Locate and identify every blood parasite.
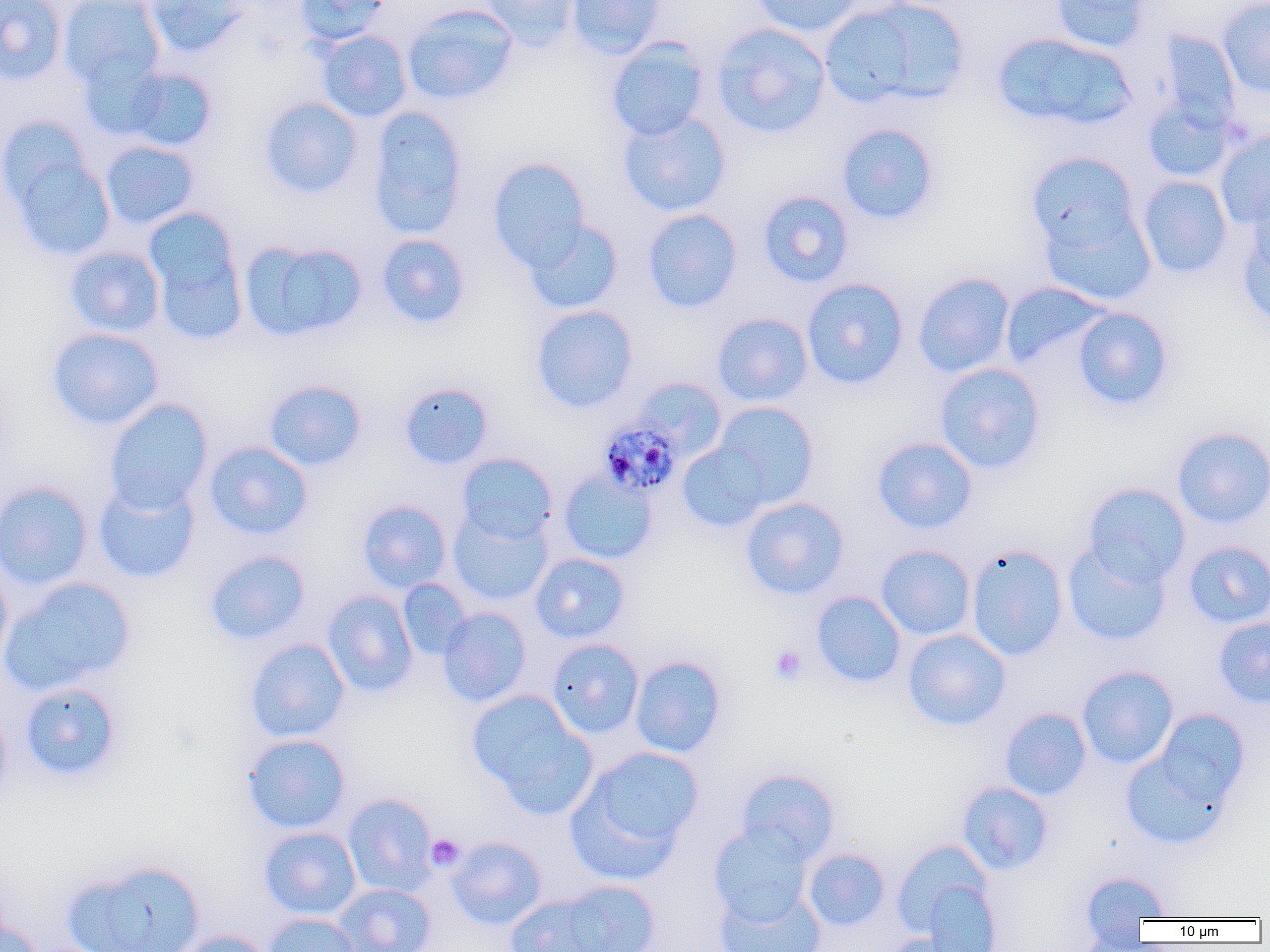

Approximate bounding boxes as named x1/y1/x2/y2 corners in pixels.
Plasmodium malariae-infected red blood cells: (x1=597, y1=417, x2=683, y2=498).
No Plasmodium falciparum, Plasmodium ovale, Plasmodium vivax, Babesia divergens, or Trypanosoma brucei observed.

slide-level diagnosis = Plasmodium malariae
platelet locations = approximate bounding boxes as named x1/y1/x2/y2 corners in pixels: (x1=769, y1=645, x2=809, y2=686), (x1=425, y1=834, x2=465, y2=872)
preparation = thin blood smear
modality = light microscopy
magnification = 1000x
image size = 1270×952 pixels
field of view = single
uninfected red blood cell locations = approximate bounding boxes as named x1/y1/x2/y2 corners in pixels: (x1=0, y1=0, x2=67, y2=86), (x1=58, y1=0, x2=166, y2=89), (x1=143, y1=0, x2=248, y2=58), (x1=295, y1=0, x2=393, y2=46), (x1=479, y1=0, x2=583, y2=48), (x1=565, y1=0, x2=666, y2=59), (x1=749, y1=0, x2=866, y2=37), (x1=819, y1=0, x2=969, y2=111), (x1=1050, y1=0, x2=1156, y2=52), (x1=1218, y1=0, x2=1270, y2=98), (x1=401, y1=4, x2=519, y2=105), (x1=711, y1=23, x2=832, y2=139), (x1=1156, y1=29, x2=1241, y2=129), (x1=317, y1=30, x2=413, y2=122), (x1=991, y1=31, x2=1137, y2=131), (x1=605, y1=37, x2=711, y2=142), (x1=77, y1=56, x2=172, y2=142), (x1=119, y1=66, x2=218, y2=152), (x1=259, y1=96, x2=363, y2=198), (x1=1142, y1=97, x2=1235, y2=184), (x1=365, y1=105, x2=469, y2=238), (x1=618, y1=110, x2=732, y2=217), (x1=835, y1=123, x2=941, y2=225), (x1=1214, y1=131, x2=1270, y2=229), (x1=4, y1=137, x2=116, y2=262), (x1=100, y1=140, x2=199, y2=230), (x1=1025, y1=151, x2=1141, y2=256), (x1=487, y1=157, x2=590, y2=271), (x1=1137, y1=175, x2=1232, y2=279), (x1=1246, y1=179, x2=1270, y2=280), (x1=757, y1=191, x2=855, y2=288), (x1=1039, y1=203, x2=1157, y2=307), (x1=641, y1=208, x2=743, y2=313), (x1=145, y1=210, x2=245, y2=341), (x1=523, y1=219, x2=624, y2=314), (x1=1237, y1=226, x2=1270, y2=328), (x1=375, y1=233, x2=471, y2=329), (x1=239, y1=238, x2=367, y2=342), (x1=64, y1=245, x2=165, y2=337), (x1=913, y1=272, x2=1016, y2=378), (x1=802, y1=277, x2=909, y2=390), (x1=999, y1=281, x2=1110, y2=369), (x1=530, y1=304, x2=639, y2=413), (x1=1072, y1=307, x2=1174, y2=411), (x1=712, y1=312, x2=814, y2=407), (x1=47, y1=327, x2=164, y2=430), (x1=934, y1=362, x2=1046, y2=475), (x1=633, y1=377, x2=728, y2=460), (x1=263, y1=379, x2=367, y2=472), (x1=399, y1=382, x2=494, y2=470), (x1=104, y1=398, x2=213, y2=512), (x1=709, y1=401, x2=819, y2=510), (x1=1171, y1=426, x2=1270, y2=529), (x1=872, y1=436, x2=978, y2=534), (x1=203, y1=440, x2=314, y2=541), (x1=677, y1=440, x2=773, y2=532), (x1=456, y1=452, x2=557, y2=545), (x1=558, y1=470, x2=658, y2=565), (x1=92, y1=477, x2=201, y2=584), (x1=1, y1=480, x2=94, y2=592), (x1=1081, y1=483, x2=1191, y2=587), (x1=740, y1=497, x2=849, y2=601), (x1=357, y1=499, x2=452, y2=593), (x1=449, y1=508, x2=553, y2=607), (x1=1062, y1=540, x2=1171, y2=646), (x1=1183, y1=541, x2=1270, y2=628), (x1=966, y1=544, x2=1069, y2=661), (x1=876, y1=545, x2=975, y2=640), (x1=203, y1=549, x2=311, y2=646), (x1=530, y1=552, x2=631, y2=644), (x1=0, y1=565, x2=13, y2=675), (x1=1, y1=576, x2=136, y2=696), (x1=397, y1=578, x2=472, y2=660), (x1=322, y1=590, x2=418, y2=697), (x1=811, y1=591, x2=906, y2=688), (x1=437, y1=607, x2=533, y2=708), (x1=1213, y1=616, x2=1270, y2=708), (x1=902, y1=629, x2=1011, y2=731), (x1=244, y1=638, x2=350, y2=743), (x1=546, y1=638, x2=644, y2=738), (x1=629, y1=655, x2=727, y2=758), (x1=1077, y1=665, x2=1179, y2=769), (x1=18, y1=682, x2=123, y2=782), (x1=466, y1=689, x2=594, y2=812), (x1=0, y1=706, x2=12, y2=808), (x1=999, y1=707, x2=1092, y2=801), (x1=1139, y1=707, x2=1250, y2=830), (x1=241, y1=733, x2=351, y2=835), (x1=569, y1=746, x2=704, y2=876), (x1=1119, y1=747, x2=1231, y2=851), (x1=735, y1=768, x2=840, y2=864), (x1=956, y1=781, x2=1054, y2=876), (x1=342, y1=793, x2=438, y2=897), (x1=709, y1=823, x2=814, y2=925), (x1=259, y1=826, x2=361, y2=920), (x1=447, y1=837, x2=546, y2=929), (x1=891, y1=839, x2=997, y2=942), (x1=802, y1=847, x2=891, y2=932), (x1=63, y1=859, x2=206, y2=952), (x1=1079, y1=871, x2=1172, y2=938), (x1=914, y1=875, x2=1004, y2=952), (x1=554, y1=880, x2=661, y2=952), (x1=332, y1=883, x2=437, y2=952), (x1=713, y1=885, x2=827, y2=952), (x1=504, y1=893, x2=613, y2=952), (x1=263, y1=912, x2=361, y2=952), (x1=0, y1=919, x2=44, y2=952), (x1=169, y1=930, x2=273, y2=952), (x1=1073, y1=931, x2=1158, y2=952), (x1=880, y1=933, x2=978, y2=952)